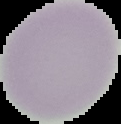

image size = 121×124 pixels
malaria status = uninfected
preparation = thin blood smear
image type = segmented cell region on a black background